Give the position of every Plasmodium parasite, noting whether each is a trophozoite, schizont, or gametocyte.
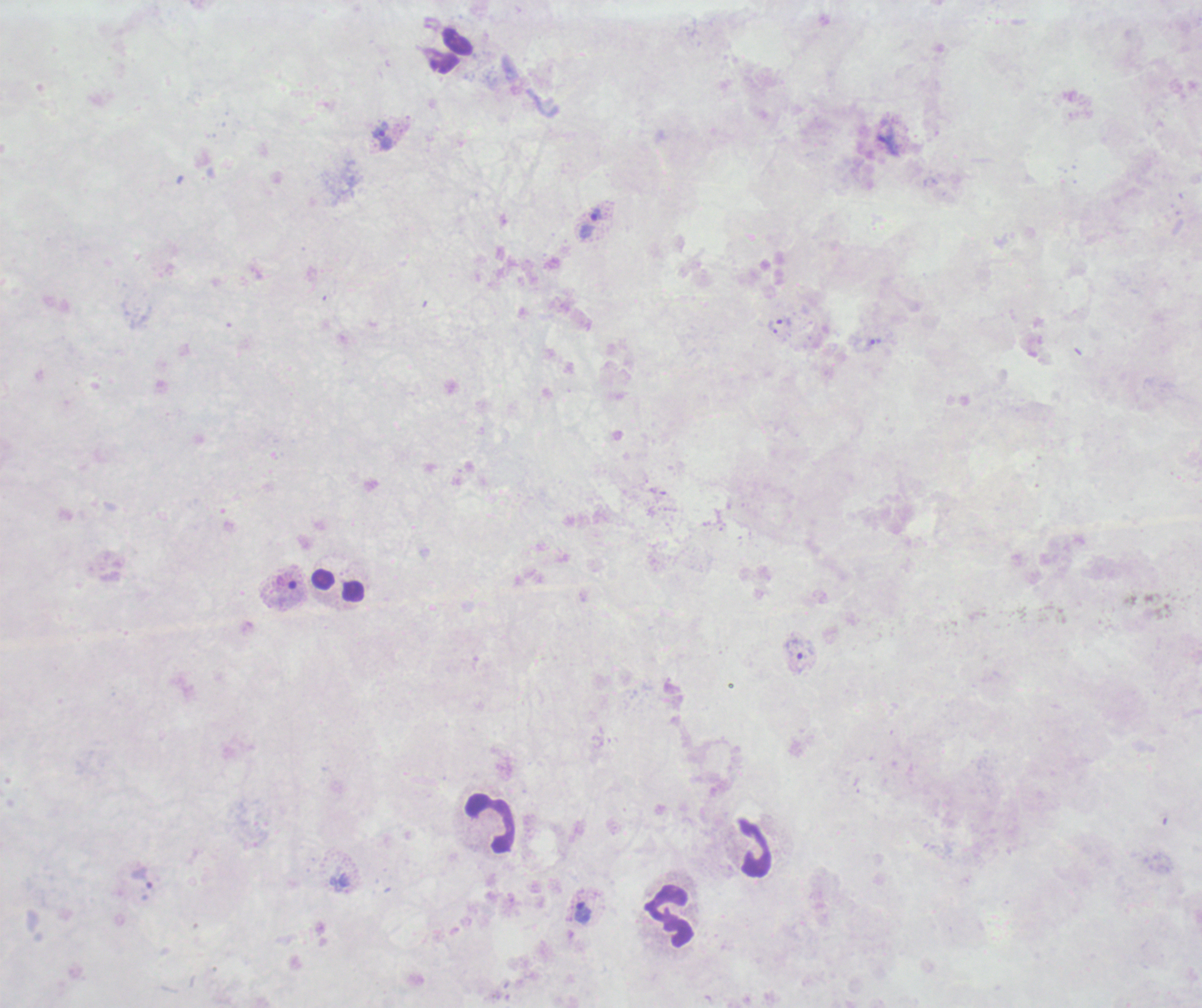
Approximate centers as {x, y} in pixels.
Trophozoites: {383, 137}, {596, 213}, {784, 321}, {772, 328}, {875, 342}, {142, 878}, {583, 913}.
No schizont or gametocyte forms observed.

Approximate centers as {x, y} in pixels.
Summary:
  - Leukocyte locations: {338, 586}, {490, 823}, {755, 848}, {668, 915}
  - Magnification: 100x
  - Coloration quality: bad
  - Field of view: single
  - Image size: 1202×1008 pixels
  - Stain: Romanowsky
  - Preparation: thick blood film
  - Context: previously used in a real diagnosis
  - Background quality: poor